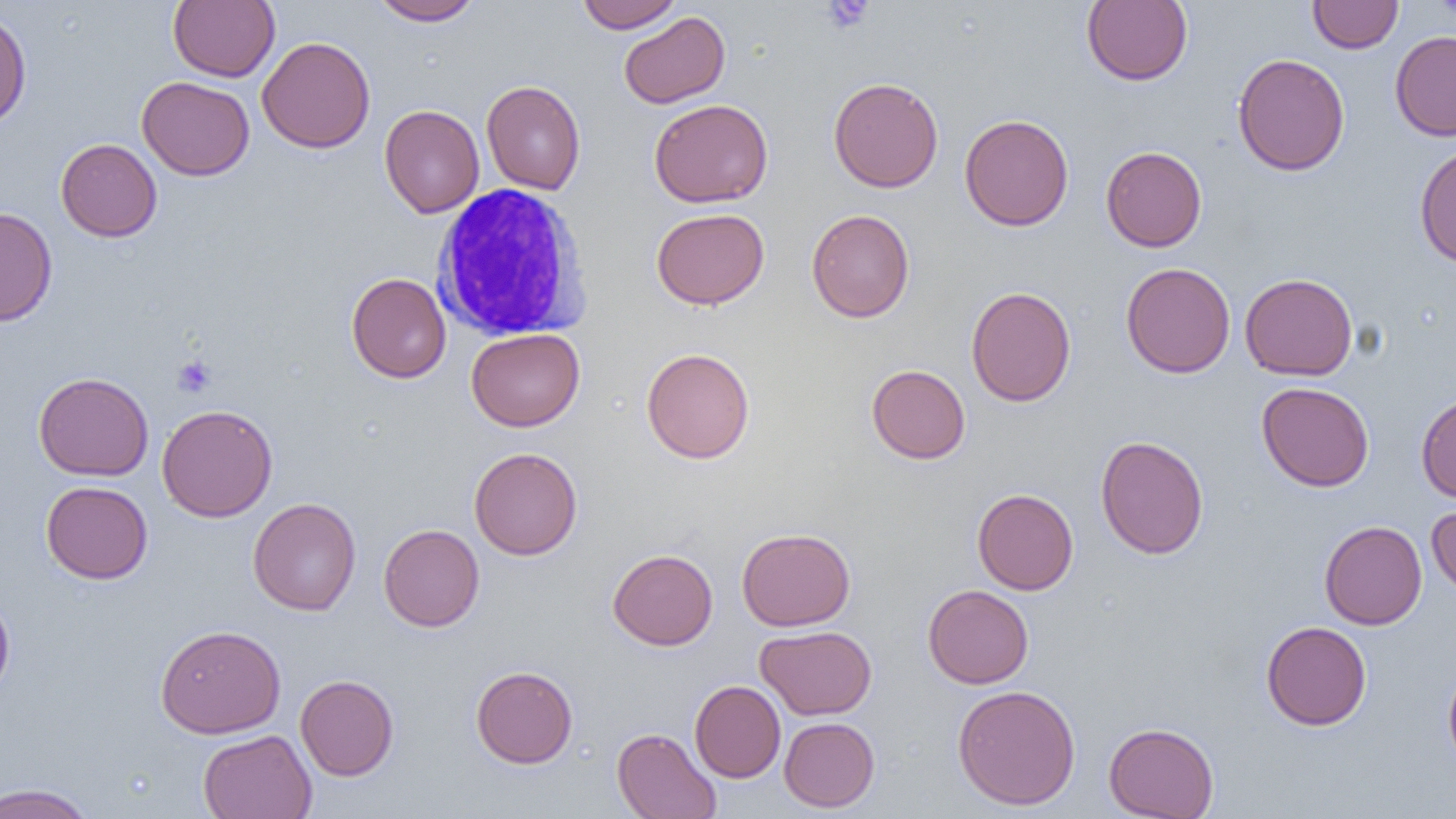

Approximate bounding boxes as (x1, y1, x2, y2) in pixels. Uninfected red blood cell locations: (168, 0, 280, 82), (369, 0, 483, 26), (574, 0, 684, 32), (1081, 0, 1193, 86), (1307, 0, 1403, 53), (1434, 0, 1456, 19), (0, 9, 31, 131), (618, 11, 730, 109), (1390, 30, 1456, 141), (257, 36, 376, 154), (1232, 53, 1349, 176), (137, 76, 255, 181), (828, 77, 944, 192), (481, 80, 586, 195), (649, 99, 773, 208), (379, 104, 484, 218), (959, 114, 1074, 231), (56, 138, 162, 242), (1414, 144, 1456, 268), (1101, 146, 1207, 252), (0, 207, 57, 327), (651, 208, 769, 309), (806, 209, 915, 322), (1120, 262, 1235, 378), (347, 273, 451, 383), (1240, 273, 1358, 380), (966, 286, 1076, 406), (466, 328, 585, 431), (642, 348, 755, 464), (866, 364, 971, 464), (33, 372, 154, 481), (1256, 382, 1375, 492), (1416, 391, 1456, 503), (157, 404, 277, 522), (1095, 435, 1209, 559), (469, 447, 583, 560), (41, 481, 153, 584), (972, 488, 1078, 595), (247, 497, 361, 616), (1426, 501, 1456, 602), (1319, 520, 1427, 629), (378, 524, 484, 632), (736, 527, 856, 631), (607, 548, 718, 650), (922, 584, 1034, 689), (0, 589, 15, 703), (1260, 621, 1372, 730), (155, 624, 286, 738), (755, 625, 877, 720), (1443, 662, 1456, 772), (470, 665, 578, 768), (295, 674, 399, 781), (689, 680, 786, 782), (952, 684, 1081, 811), (779, 717, 880, 812), (1104, 722, 1219, 818), (612, 727, 721, 819), (197, 729, 318, 819), (0, 782, 98, 819). Platelet locations: (821, 0, 874, 33), (172, 355, 216, 397). White blood cell locations: (430, 184, 593, 341). Slide-level diagnosis: no evidence of blood parasites. Light microscopy. Single field of view. 1000x magnification. Image is 1456×819 pixels. Thin blood smear.